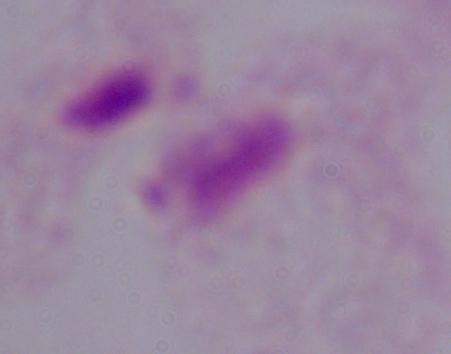

Summary:
  - Identification: trichomonad
  - Modality: micrograph
  - Magnification: 1000x